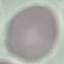
Summary:
  - Malaria status: uninfected
  - Capture: smartphone through the microscope eyepiece
  - Stain: Giemsa
  - Preparation: thin blood film
  - Image type: automatically extracted cell patch, resized to 64 × 64 pixels